Give the position of every leukocyte visible.
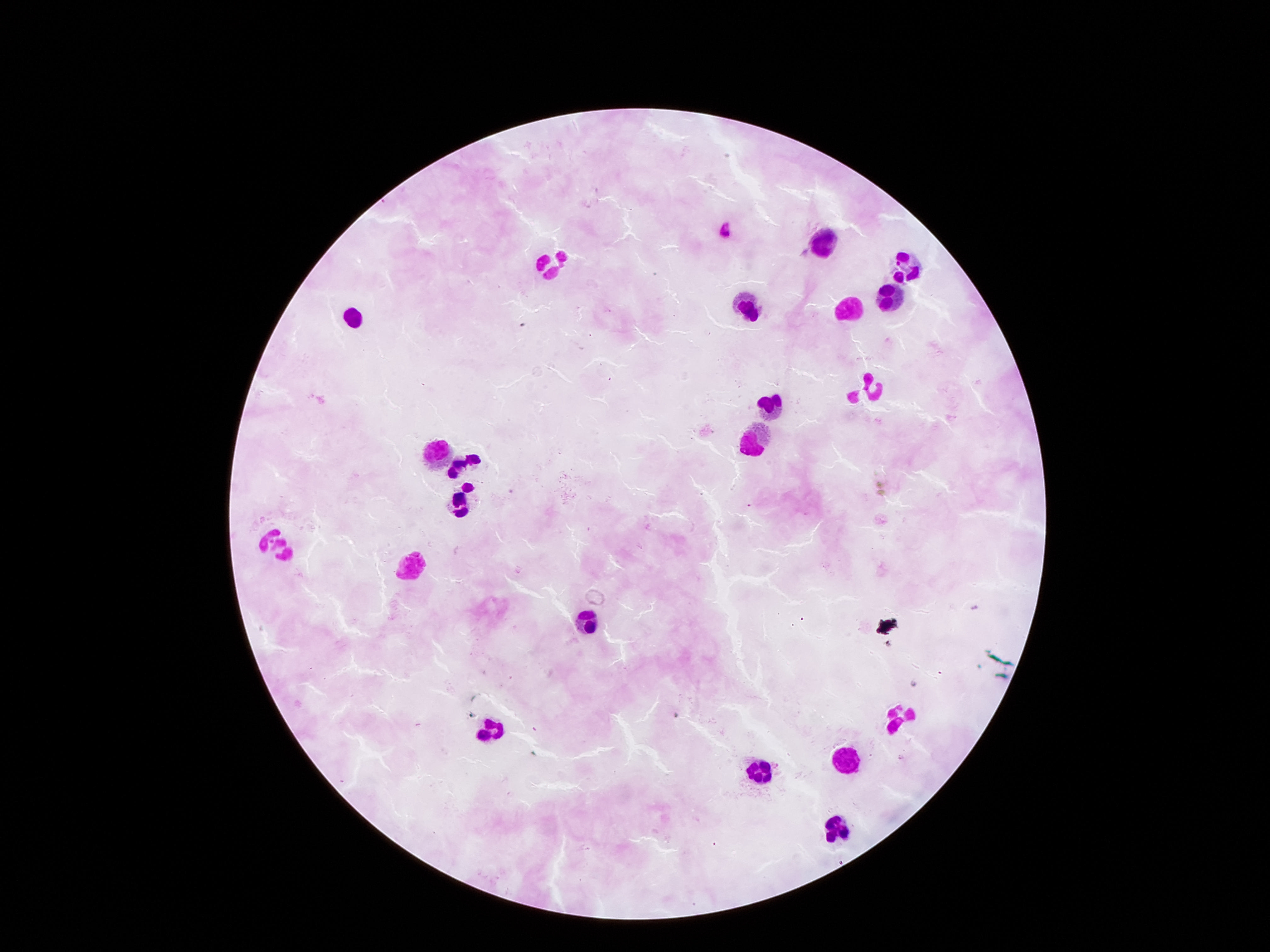
Approximate object centers, in pixels from the top-left corner.
Leukocytes: (x=829, y=238), (x=552, y=262), (x=910, y=264), (x=890, y=300), (x=752, y=304), (x=848, y=308), (x=354, y=318), (x=867, y=386), (x=772, y=401), (x=754, y=440), (x=435, y=451), (x=469, y=464), (x=463, y=500), (x=276, y=549), (x=412, y=564), (x=589, y=628), (x=901, y=720), (x=493, y=728), (x=847, y=759), (x=759, y=772), (x=834, y=826).

Summary:
  - Field of view: one from this slide
  - Magnification: 100x
  - Preparation: thick blood film
  - Capture: smartphone camera through the microscope eyepiece
  - Stain: Giemsa
  - Patient malaria status: negative
  - Image size: 1270×952 pixels